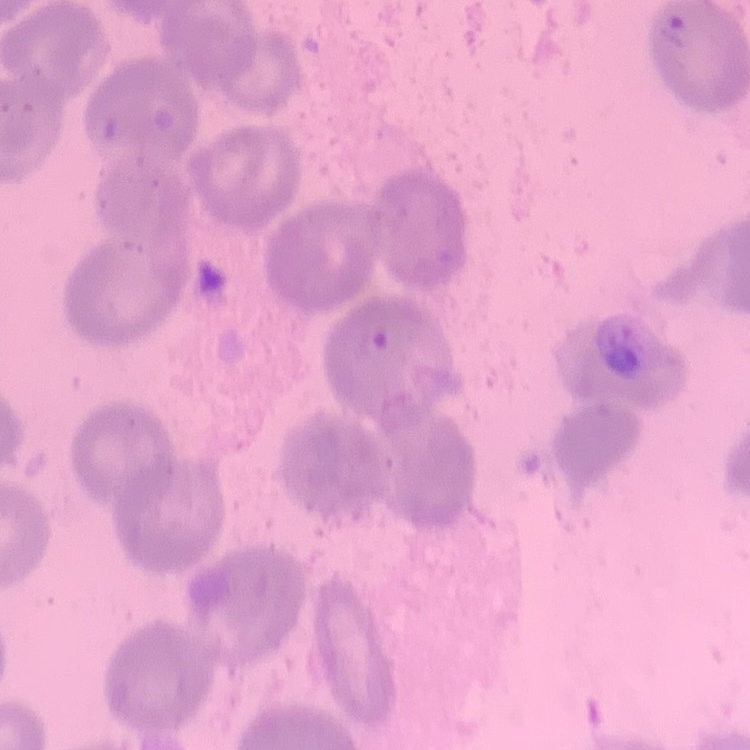

Summary:
  - Red blood cell morphology: no rouleaux formation
  - Image type: square crop of a larger photomicrograph
  - Stain: Field's or Giemsa
  - Preparation: thin blood film